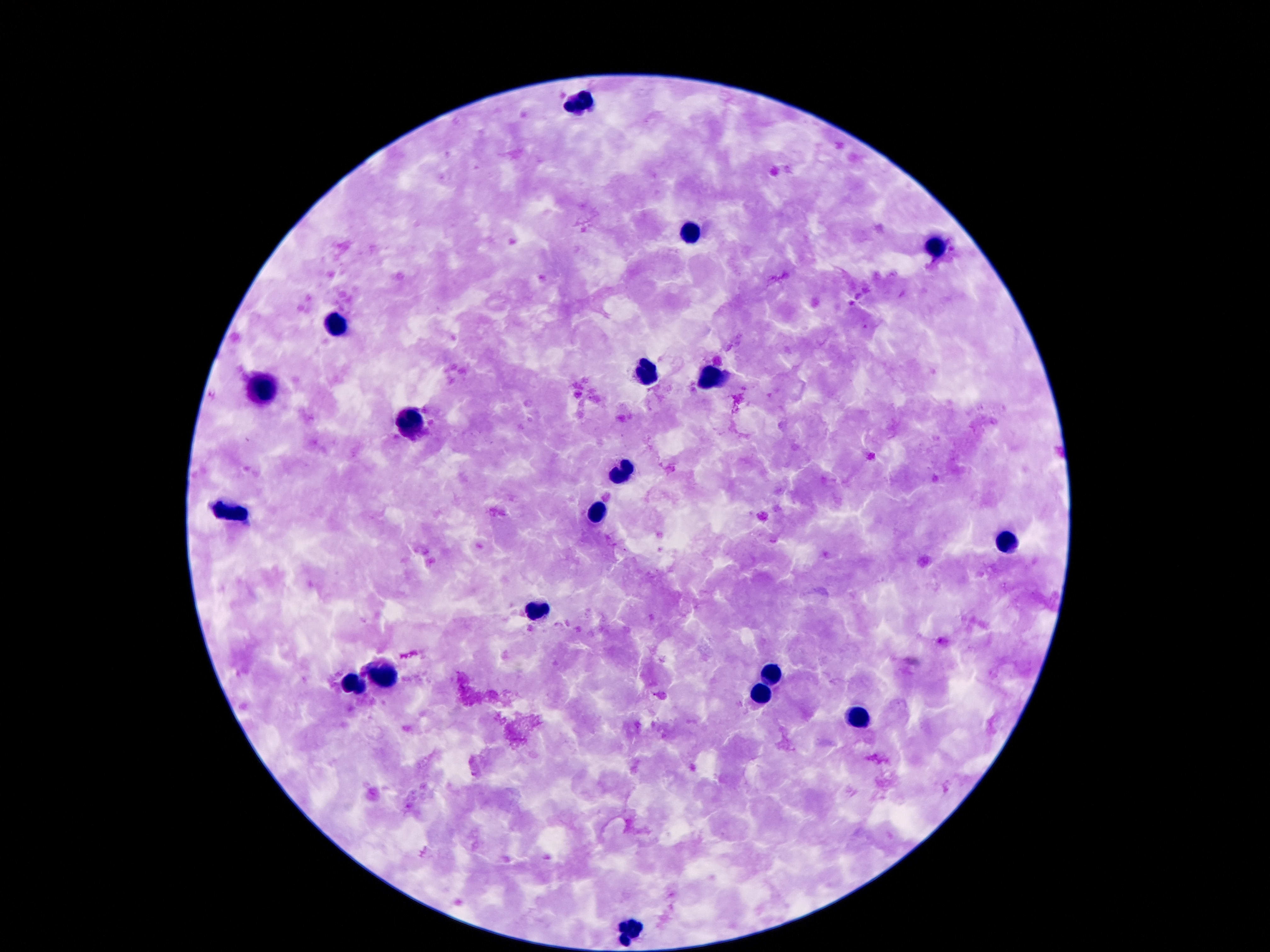

Approximate centers as [x, y] in pixels. Leukocyte locations: [582, 103], [691, 232], [936, 249], [335, 322], [647, 370], [712, 377], [260, 387], [412, 424], [624, 471], [229, 510], [596, 512], [1007, 541], [533, 611], [382, 671], [772, 674], [352, 683], [761, 694], [858, 717], [629, 928]. Smartphone photograph taken through the microscope eyepiece. Image is 1270×952 pixels. Giemsa stain. 100x magnification. Thick blood film. Patient malaria status: negative. One field from this slide.